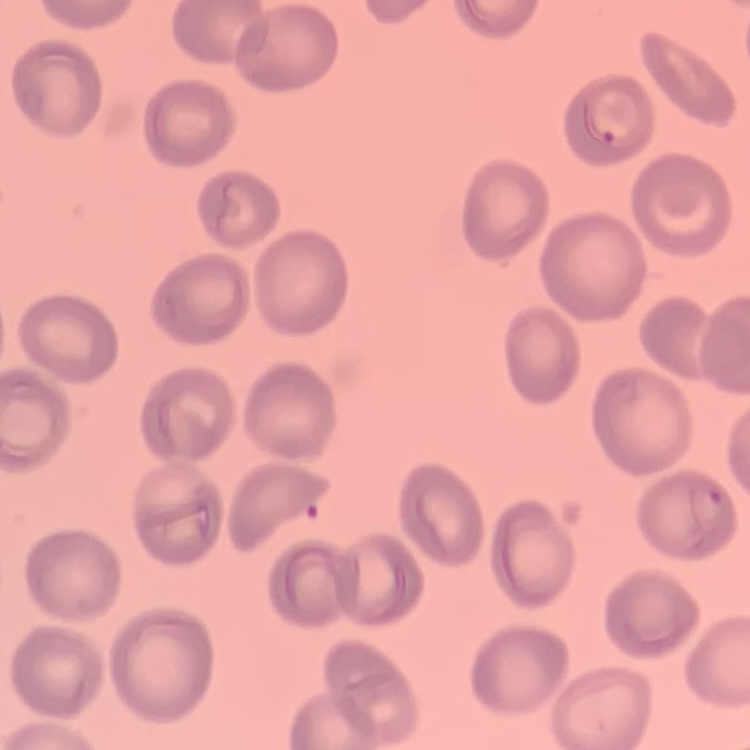

Summary:
  - Erythrocyte morphology: no rouleaux formation
  - Image type: square crop of a larger photomicrograph
  - Stain: Field's or Giemsa
  - Preparation: thin blood smear